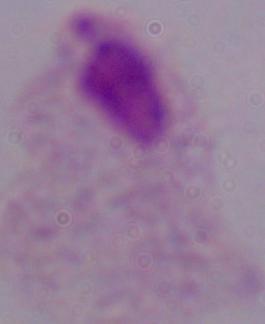
1000x magnification. A trichomonad is shown. Micrograph.